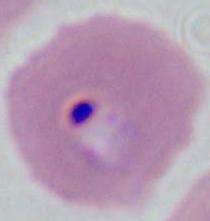
Summary:
  - Modality: micrograph
  - Magnification: 400x or 1000x
  - Identification: Plasmodium